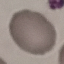

Summary:
  - Malaria status: uninfected
  - Stain: Giemsa
  - Image type: automatically extracted cell patch, resized to 64 × 64 pixels
  - Preparation: thin smear
  - Capture: smartphone camera at the microscope eyepiece